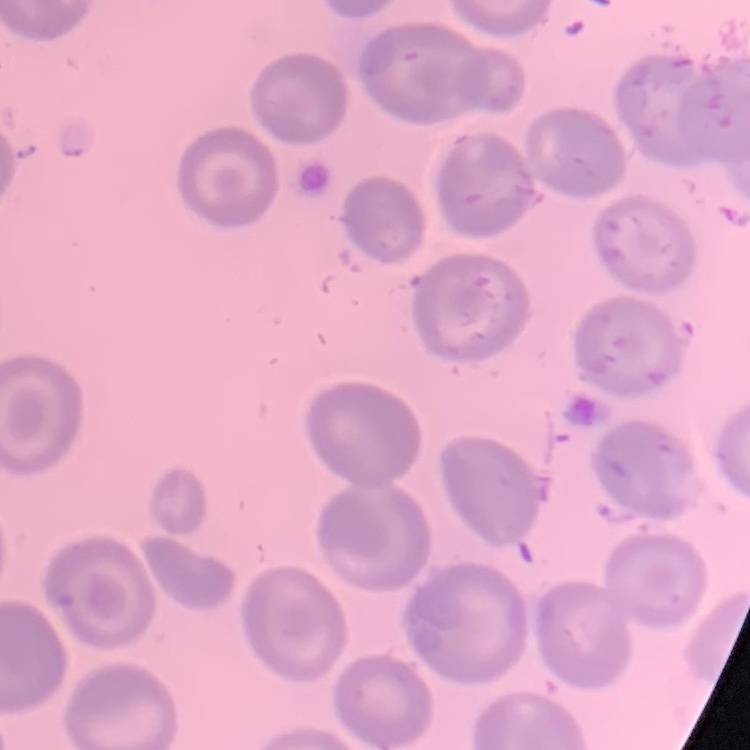

red_blood_cell_morphology: no rouleaux formation
preparation: thin blood smear
stain: Field's or Giemsa
image_type: square crop of a larger photomicrograph